Identify the blood parasite species.
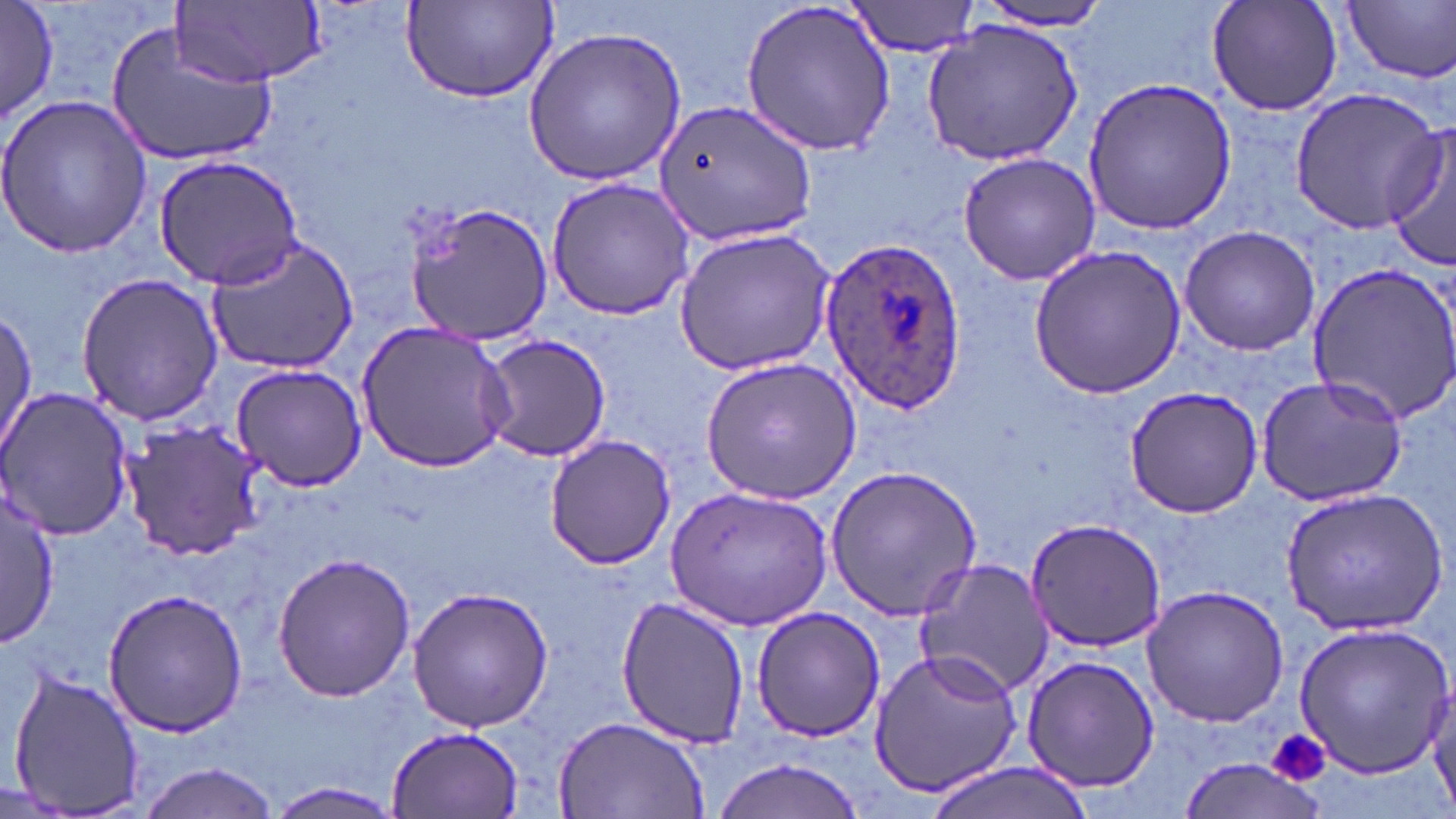
Plasmodium ovale.

Approximate bounding boxes as [x1, y1, x2, y2] in pixels. Uninfected red blood cell locations: [1, 0, 58, 127], [173, 0, 326, 87], [400, 0, 561, 106], [848, 0, 983, 57], [1206, 0, 1345, 119], [740, 1, 897, 155], [1344, 1, 1456, 83], [969, 3, 1119, 31], [107, 20, 278, 168], [920, 20, 1085, 164], [519, 27, 687, 188], [1081, 76, 1236, 237], [1287, 87, 1444, 234], [0, 92, 154, 259], [650, 97, 817, 247], [1384, 125, 1456, 274], [956, 150, 1102, 286], [156, 154, 303, 288], [546, 177, 699, 320], [402, 201, 555, 347], [1178, 223, 1321, 357], [673, 228, 837, 376], [205, 235, 359, 375], [1030, 246, 1186, 399], [1304, 258, 1456, 429], [75, 272, 225, 427], [1, 309, 37, 459], [355, 320, 516, 475], [476, 334, 615, 462], [700, 356, 860, 503], [228, 362, 369, 493], [1254, 375, 1410, 506], [1, 385, 135, 541], [1123, 385, 1262, 519], [116, 420, 266, 560], [543, 432, 676, 570], [824, 466, 985, 621], [665, 486, 833, 633], [1280, 487, 1446, 634], [2, 491, 61, 650], [1023, 517, 1170, 653], [270, 551, 415, 703], [914, 558, 1055, 697], [406, 584, 555, 733], [1140, 584, 1291, 728], [101, 587, 249, 736], [615, 594, 750, 749], [750, 605, 886, 740], [1293, 621, 1452, 778], [869, 647, 1025, 798], [1019, 654, 1161, 793], [7, 665, 147, 816], [1425, 683, 1456, 814], [554, 714, 710, 819], [386, 724, 526, 819], [711, 755, 870, 819], [1175, 759, 1328, 817], [137, 760, 281, 819], [922, 762, 1095, 819], [267, 780, 402, 817]. Platelet locations: [1268, 727, 1332, 790]. Plasmodium ovale-infected red blood cell locations: [820, 239, 968, 418]. Image is 1456×819 pixels. One field of a larger specimen. May-Grünwald-Giemsa stain. Light microscopy. Captured at 1000x magnification. Thin blood smear.